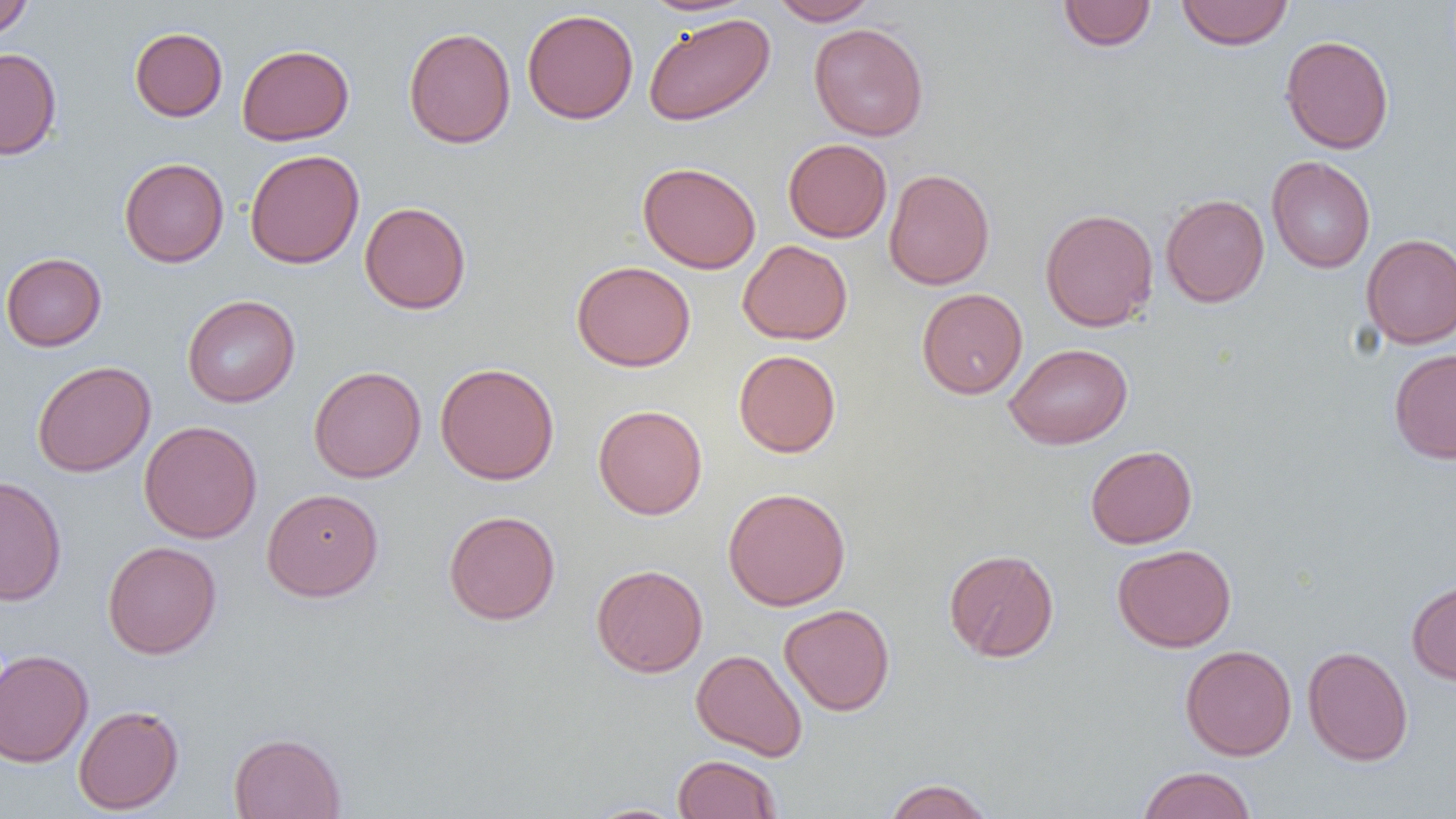
Summary:
  - Coordinate format: approximate bounding boxes as named x1/y1/x2/y2 corners in pixels
  - Uninfected red blood cell locations: (x1=0, y1=0, x2=34, y2=39), (x1=638, y1=0, x2=757, y2=17), (x1=769, y1=0, x2=879, y2=25), (x1=1177, y1=0, x2=1293, y2=50), (x1=1057, y1=1, x2=1157, y2=51), (x1=522, y1=8, x2=638, y2=124), (x1=643, y1=13, x2=775, y2=126), (x1=809, y1=23, x2=929, y2=141), (x1=403, y1=26, x2=516, y2=149), (x1=129, y1=27, x2=227, y2=122), (x1=1280, y1=34, x2=1394, y2=154), (x1=237, y1=44, x2=354, y2=145), (x1=0, y1=48, x2=62, y2=160), (x1=783, y1=138, x2=892, y2=243), (x1=244, y1=149, x2=365, y2=269), (x1=1266, y1=156, x2=1376, y2=273), (x1=119, y1=158, x2=229, y2=267), (x1=637, y1=161, x2=762, y2=273), (x1=883, y1=168, x2=995, y2=290), (x1=1160, y1=194, x2=1269, y2=307), (x1=359, y1=201, x2=471, y2=315), (x1=1040, y1=208, x2=1159, y2=332), (x1=1361, y1=233, x2=1456, y2=348), (x1=737, y1=240, x2=853, y2=345), (x1=1, y1=252, x2=107, y2=351), (x1=571, y1=260, x2=696, y2=371), (x1=916, y1=288, x2=1028, y2=398), (x1=182, y1=295, x2=300, y2=407), (x1=1004, y1=343, x2=1133, y2=449), (x1=1388, y1=348, x2=1456, y2=464), (x1=733, y1=349, x2=841, y2=457), (x1=31, y1=360, x2=156, y2=477), (x1=435, y1=362, x2=560, y2=485), (x1=308, y1=365, x2=426, y2=483), (x1=593, y1=405, x2=708, y2=519), (x1=139, y1=421, x2=262, y2=543), (x1=1085, y1=444, x2=1198, y2=548), (x1=0, y1=475, x2=67, y2=606), (x1=722, y1=486, x2=851, y2=611), (x1=261, y1=487, x2=384, y2=602), (x1=444, y1=509, x2=561, y2=625), (x1=102, y1=540, x2=222, y2=659), (x1=1112, y1=543, x2=1237, y2=652), (x1=943, y1=548, x2=1059, y2=662), (x1=591, y1=563, x2=708, y2=677), (x1=1407, y1=579, x2=1456, y2=686), (x1=779, y1=603, x2=895, y2=716), (x1=1180, y1=644, x2=1297, y2=760), (x1=1302, y1=645, x2=1413, y2=766), (x1=0, y1=649, x2=93, y2=768), (x1=690, y1=649, x2=808, y2=761), (x1=73, y1=704, x2=184, y2=815), (x1=229, y1=732, x2=346, y2=819), (x1=672, y1=753, x2=782, y2=819), (x1=1137, y1=766, x2=1256, y2=819), (x1=882, y1=778, x2=995, y2=819), (x1=583, y1=803, x2=690, y2=818)
  - Slide-level diagnosis: no evidence of blood parasites
  - Magnification: 1000x
  - Field of view: one of a larger specimen
  - Image size: 1456×819 pixels
  - Modality: optical microscopy
  - Preparation: thin blood smear